Classify this cell by malaria status.
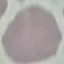
Uninfected.

Summary:
  - Image type: cell patch, automatically extracted from a larger field of view and resized to 64 × 64 pixels
  - Stain: Giemsa
  - Capture: smartphone camera at the microscope eyepiece
  - Preparation: thin smear